Classify this cell by malaria status.
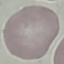

It is uninfected.

stain: Giemsa
image_type: cell patch, automatically extracted from a larger field of view and resized to 64 × 64 pixels
capture: smartphone through the microscope eyepiece
preparation: thin blood smear